Locate every blood parasite and identify its species.
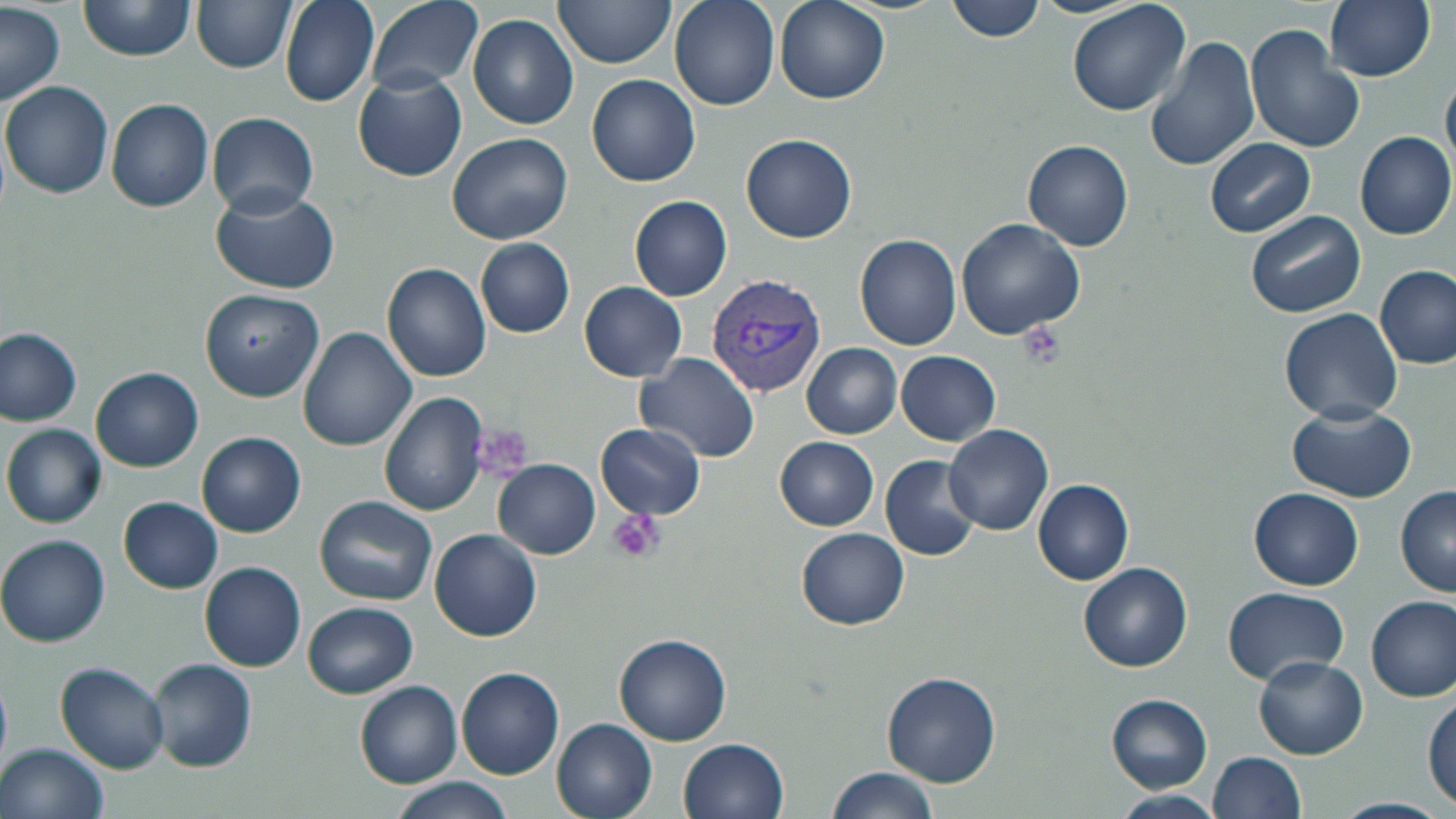

Approximate bounding boxes as [x1, y1, x2, y2] in pixels.
Plasmodium vivax-infected red blood cells: [704, 274, 828, 398].
No Plasmodium falciparum, Plasmodium ovale, Plasmodium malariae, Babesia divergens, or Trypanosoma brucei observed.

Platelet locations: [1017, 321, 1064, 371], [480, 424, 531, 476], [605, 509, 663, 563]. Uninfected red blood cell locations: [78, 0, 197, 61], [281, 0, 381, 107], [367, 0, 484, 93], [552, 0, 677, 68], [670, 0, 779, 111], [776, 0, 890, 104], [947, 0, 1046, 43], [1030, 0, 1142, 17], [1064, 0, 1192, 117], [1323, 0, 1435, 81], [192, 1, 297, 72], [0, 3, 64, 104], [467, 13, 580, 130], [1246, 25, 1364, 154], [1145, 34, 1262, 174], [352, 70, 467, 182], [588, 73, 700, 186], [1442, 76, 1456, 168], [1, 81, 114, 199], [107, 99, 213, 212], [207, 112, 317, 216], [1355, 132, 1456, 240], [445, 133, 573, 245], [740, 134, 857, 243], [1205, 138, 1316, 237], [1024, 141, 1133, 251], [210, 185, 340, 292], [629, 196, 731, 301], [1245, 209, 1366, 319], [955, 218, 1085, 339], [854, 234, 962, 350], [475, 236, 575, 338], [383, 263, 493, 383], [1375, 264, 1454, 369], [578, 282, 688, 381], [200, 289, 325, 401], [1280, 307, 1402, 421], [297, 326, 417, 449], [0, 327, 81, 426], [802, 344, 901, 438], [896, 350, 1001, 446], [636, 352, 762, 464], [92, 367, 203, 471], [379, 392, 488, 516], [1287, 404, 1417, 504], [597, 423, 706, 521], [2, 424, 105, 528], [943, 425, 1053, 536], [198, 432, 305, 537], [775, 437, 879, 530], [880, 456, 982, 561], [493, 459, 600, 559], [1033, 478, 1133, 584], [1395, 486, 1456, 597], [1251, 488, 1363, 590], [315, 494, 437, 605], [118, 497, 222, 593], [797, 527, 910, 630], [429, 529, 541, 641], [0, 536, 110, 647], [199, 561, 307, 671], [1079, 563, 1191, 671], [1222, 587, 1349, 685], [1368, 596, 1455, 701], [303, 601, 417, 697], [614, 633, 732, 746], [1253, 656, 1368, 759], [150, 659, 256, 771], [57, 662, 171, 774], [457, 667, 564, 779], [881, 672, 1002, 788], [355, 681, 463, 788], [1422, 692, 1454, 808], [1106, 694, 1213, 793], [552, 718, 660, 819], [678, 737, 788, 819], [3, 743, 109, 819], [1210, 753, 1308, 818], [826, 765, 941, 819], [386, 776, 516, 819], [1108, 792, 1227, 818], [1328, 798, 1450, 819]. Slide-level diagnosis: Plasmodium vivax. Thin blood smear. Optical microscopy. Captured at 1000x magnification. May-Grünwald-Giemsa-stained preparation. Image is 1456×819 pixels. One field of a larger specimen.